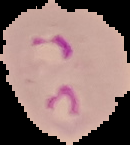 Image is 130×145 pixels. From a thin blood smear. Result: Plasmodium parasites detected. Cell region segmented out of the field of view; the surrounding area is masked to black.